Name the cell type shown.
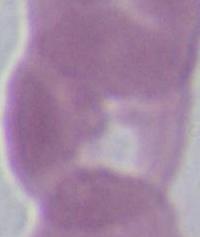
This is an erythrocyte.

modality = micrograph
magnification = 1000x